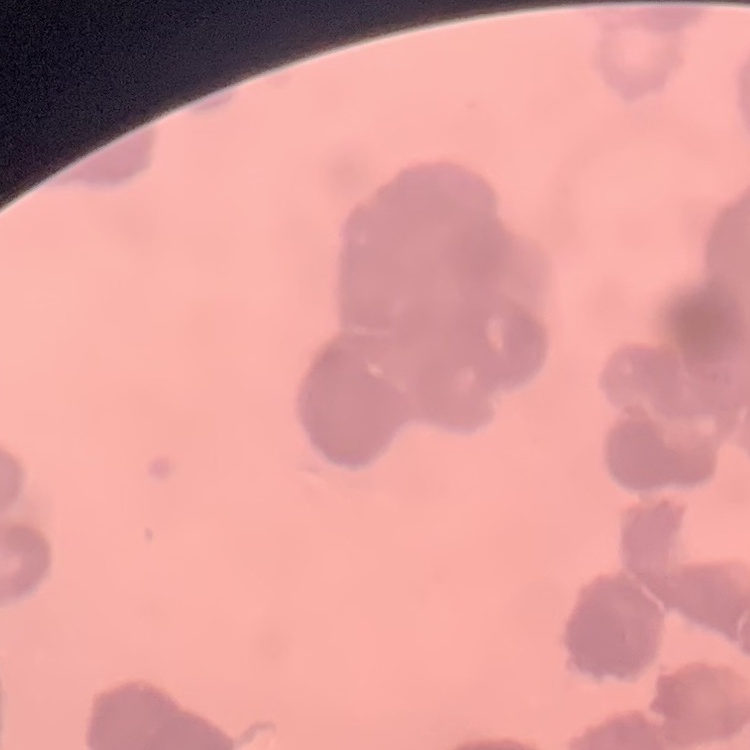
{
  "erythrocyte_morphology": "rouleaux formation",
  "image_type": "square crop of a larger photomicrograph",
  "preparation": "thin blood film",
  "stain": "Field's or Giemsa"
}